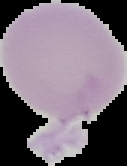
Summary:
  - Result: no malaria parasites detected
  - Image size: 127×166 pixels
  - Preparation: thin blood film
  - Image type: cell region segmented out of the field of view; surrounding area masked to black